Give the extent of all uninfected red blood cells.
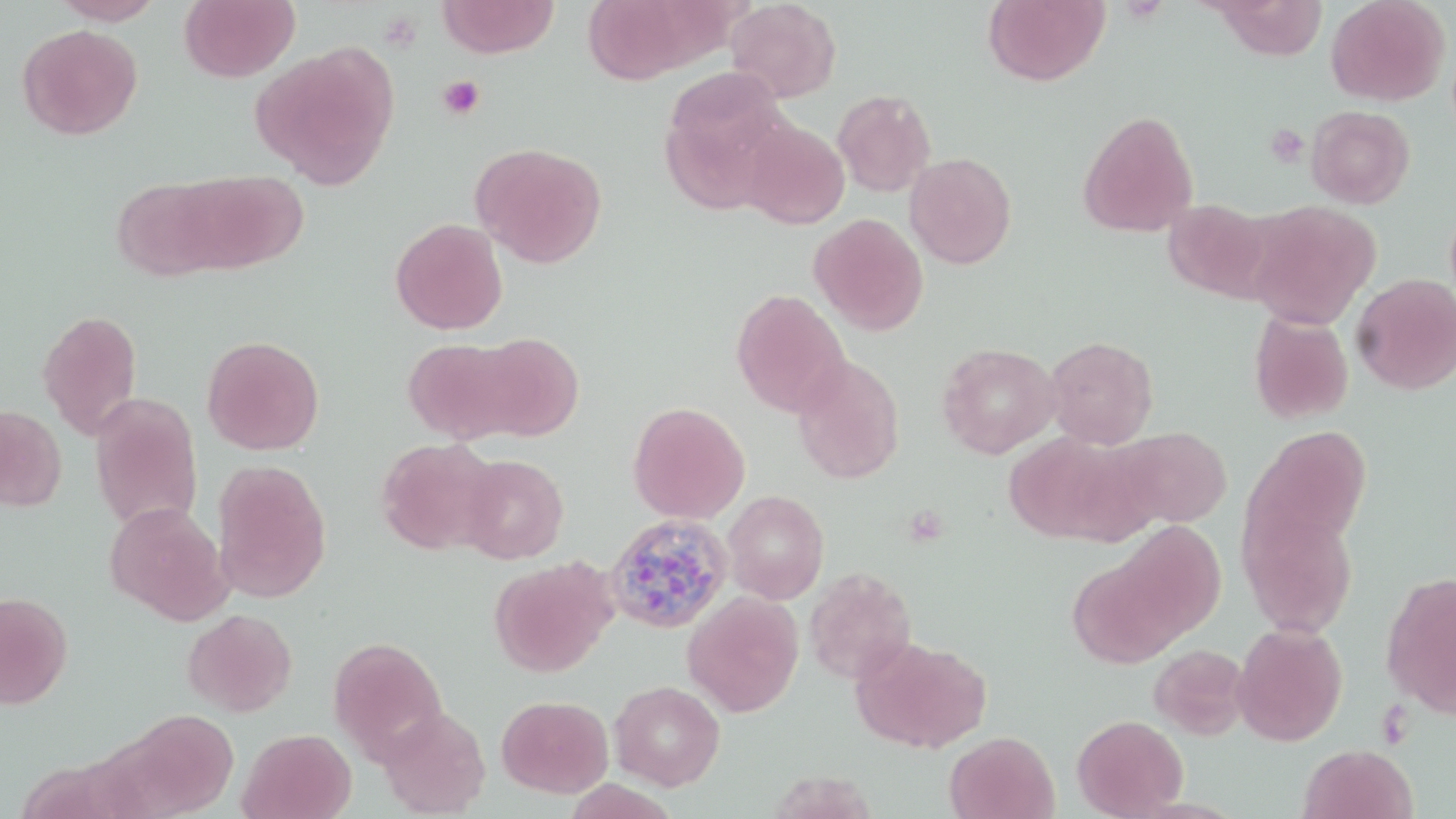

Approximate bounding boxes as [x1, y1, x2, y2] in pixels.
Uninfected red blood cells: [51, 0, 164, 26], [179, 0, 300, 82], [438, 0, 559, 58], [582, 0, 703, 84], [726, 0, 842, 103], [983, 0, 1110, 86], [1210, 0, 1329, 61], [1326, 0, 1451, 106], [16, 23, 143, 140], [252, 43, 399, 190], [659, 72, 792, 213], [832, 89, 936, 197], [1306, 105, 1415, 208], [1077, 109, 1199, 237], [735, 119, 850, 230], [470, 142, 607, 268], [904, 152, 1017, 269], [176, 170, 307, 273], [112, 177, 231, 280], [1162, 199, 1273, 301], [1243, 200, 1379, 329], [808, 213, 929, 335], [390, 218, 508, 335], [1352, 272, 1456, 395], [730, 288, 850, 418], [37, 309, 143, 440], [1248, 311, 1354, 425], [468, 332, 585, 441], [202, 335, 325, 455], [1044, 336, 1159, 449], [402, 338, 523, 443], [937, 342, 1062, 459], [791, 355, 905, 485], [89, 391, 204, 532], [627, 401, 750, 523], [0, 404, 67, 512], [1112, 426, 1233, 529], [1244, 426, 1372, 555], [1003, 432, 1144, 546], [373, 437, 503, 556], [457, 454, 569, 564], [211, 458, 333, 603], [723, 490, 829, 604], [104, 501, 232, 624], [1238, 503, 1359, 637], [1113, 521, 1226, 643], [1068, 552, 1186, 669], [488, 557, 617, 677], [803, 567, 917, 685], [1380, 571, 1456, 717], [682, 590, 805, 717], [0, 591, 73, 710], [182, 608, 298, 717], [1232, 622, 1348, 746], [327, 635, 449, 760], [851, 636, 991, 753], [1148, 644, 1250, 739], [609, 679, 725, 790], [496, 695, 614, 798], [378, 706, 492, 817], [115, 709, 240, 817], [1071, 714, 1188, 818], [239, 728, 357, 819], [944, 731, 1059, 819], [1298, 743, 1417, 819].

slide-level diagnosis = Plasmodium ovale
platelet locations = approximate bounding boxes as [x1, y1, x2, y2] in pixels: [437, 75, 485, 120], [1265, 123, 1310, 167]
preparation = thin blood smear
image size = 1456×819 pixels
modality = light microscopy
stain = May-Grünwald-Giemsa
magnification = 1000x
field of view = one of a larger specimen
Plasmodium ovale-infected red blood cell locations = approximate bounding boxes as [x1, y1, x2, y2] in pixels: [604, 513, 733, 635]